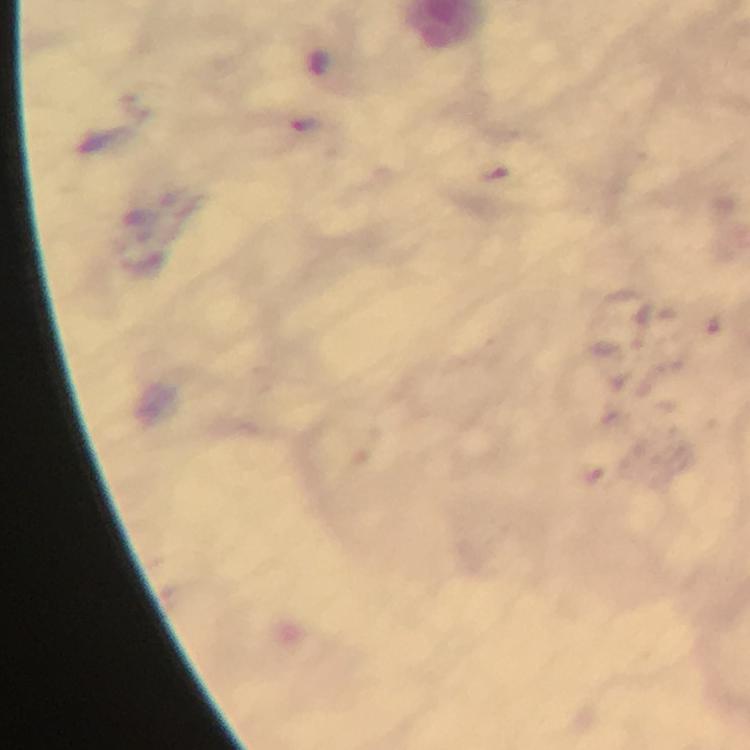
immersion oil = applied
context = from a malaria diagnostic workup
stain = Giemsa
magnification = 100x
capture = smartphone photograph through a microscope
image size = 750×750 pixels
cropped from = one field of view
malaria parasite locations = approximate centers as (x, y) in pixels: (599, 472)
preparation = thick smear